Assess this cell for malaria.
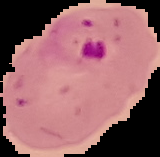
It is parasitized.

Summary:
  - Image type: cell region segmented out of the field of view; surrounding area masked to black
  - Preparation: thin blood smear
  - Image size: 160×157 pixels